Describe the morphology of the erythrocytes.
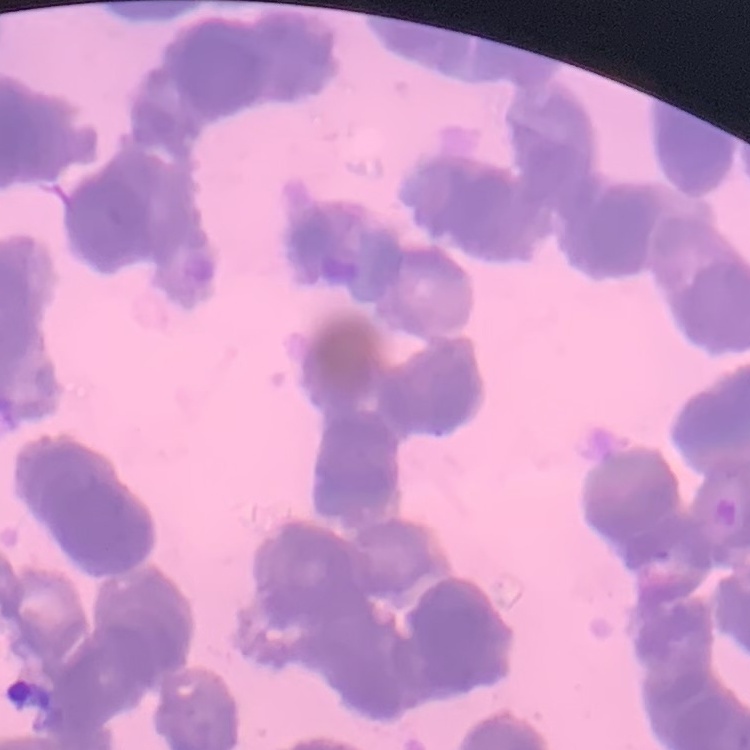

Rouleaux formation.

Field's or Giemsa stain. One tile cut from a larger photomicrograph. Thin peripheral smear.